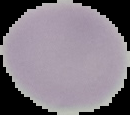

The area outside the segmented cell region is set to black. Image is 130×115 pixels. From a thin blood film. Malaria status: uninfected.